Report the malaria status of this cell.
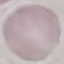
Uninfected.

preparation = thin blood film
capture = smartphone camera at the microscope eyepiece
image type = automatically extracted cell patch, resized to 64 × 64 pixels
stain = Giemsa